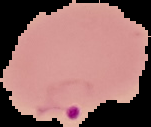
Summary:
  - Malaria status: parasitized
  - Image size: 151×127 pixels
  - Image type: segmented cell region with the area outside set to black
  - Preparation: thin blood film